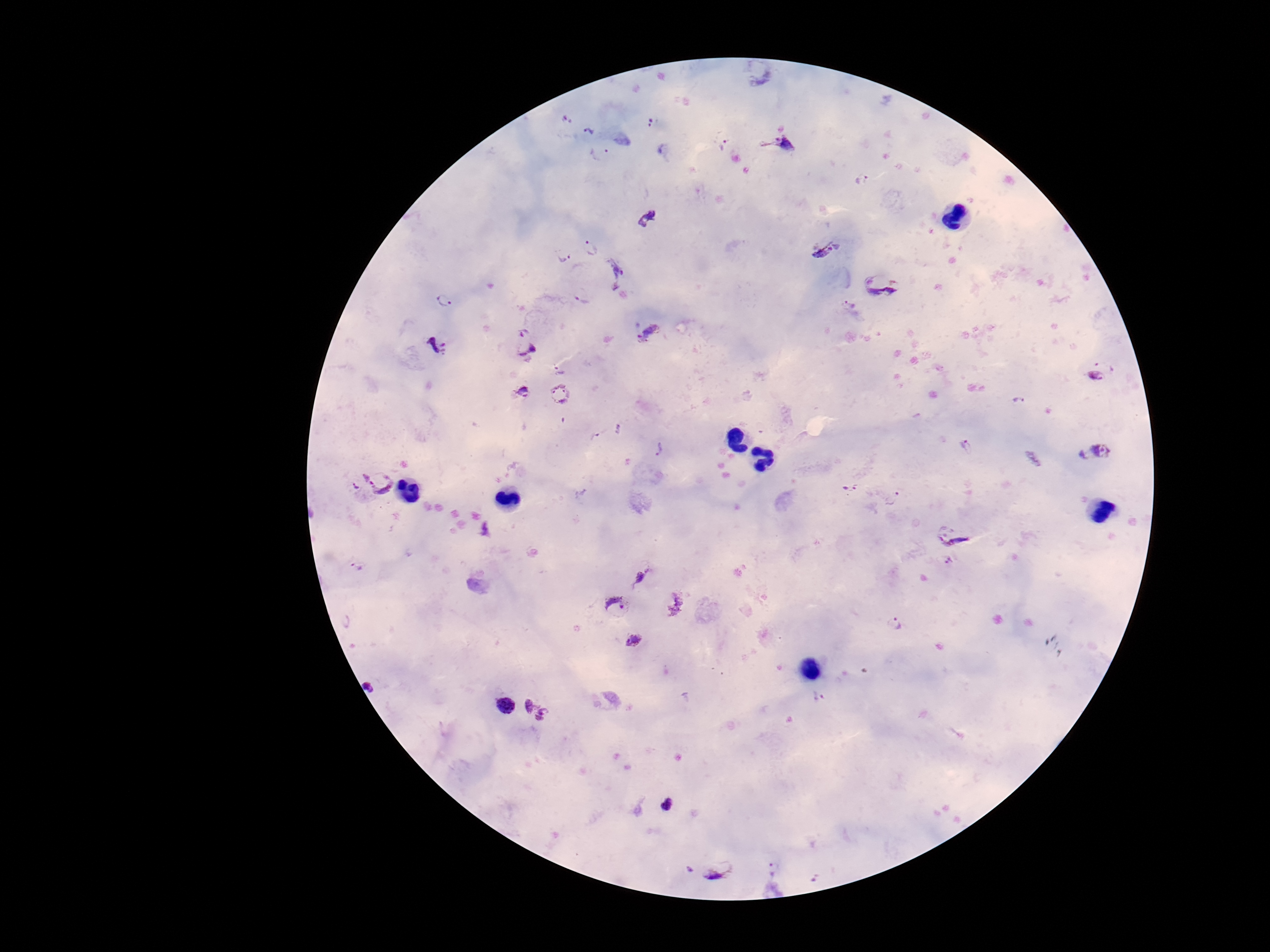

Approximate centers as [x, y] in pixels.
Summary:
  - Plasmodium parasite locations: [757, 75], [566, 117], [652, 123], [590, 131], [721, 139], [778, 142], [601, 156], [861, 179], [648, 218], [822, 243], [592, 247], [563, 254], [618, 274], [882, 281], [582, 294], [445, 300], [848, 308], [648, 333], [524, 343], [437, 345], [1108, 356], [559, 368], [1089, 382], [520, 392], [558, 394], [1019, 402], [620, 430], [597, 436], [966, 445], [659, 448], [1097, 450], [358, 479], [382, 480], [849, 486], [891, 497], [951, 533], [951, 564], [363, 568], [642, 576], [615, 605], [346, 621], [895, 624], [634, 640], [374, 683], [504, 704], [535, 708], [668, 805], [773, 867], [688, 869], [719, 869]
  - Capture: smartphone camera through the microscope eyepiece
  - Preparation: thick blood smear
  - Field of view: one from this slide
  - Patient malaria status: infected
  - Image size: 1270×952 pixels
  - Magnification: 100x
  - Stain: Giemsa